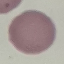

Summary:
  - Result: no malaria parasites seen
  - Image type: automatically extracted cell patch, resized to 64 × 64 pixels
  - Preparation: thin blood film
  - Stain: Giemsa
  - Capture: smartphone through the microscope eyepiece